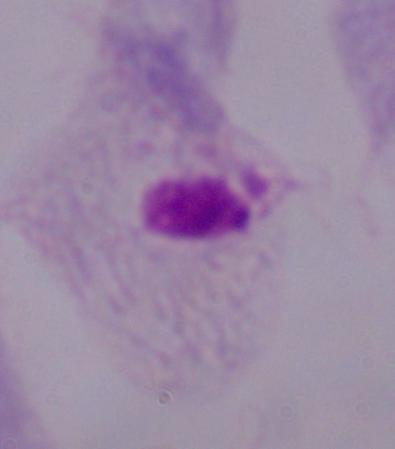

Summary:
  - Identification: trichomonad
  - Magnification: 1000x
  - Modality: photomicrograph